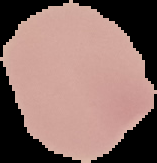

Summary:
  - Preparation: thin blood film
  - Result: no malaria parasites detected
  - Image size: 157×163 pixels
  - Image type: segmented cell region on a black background